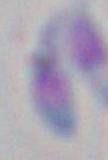

magnification = 1000x
modality = micrograph
identification = Toxoplasma gondii